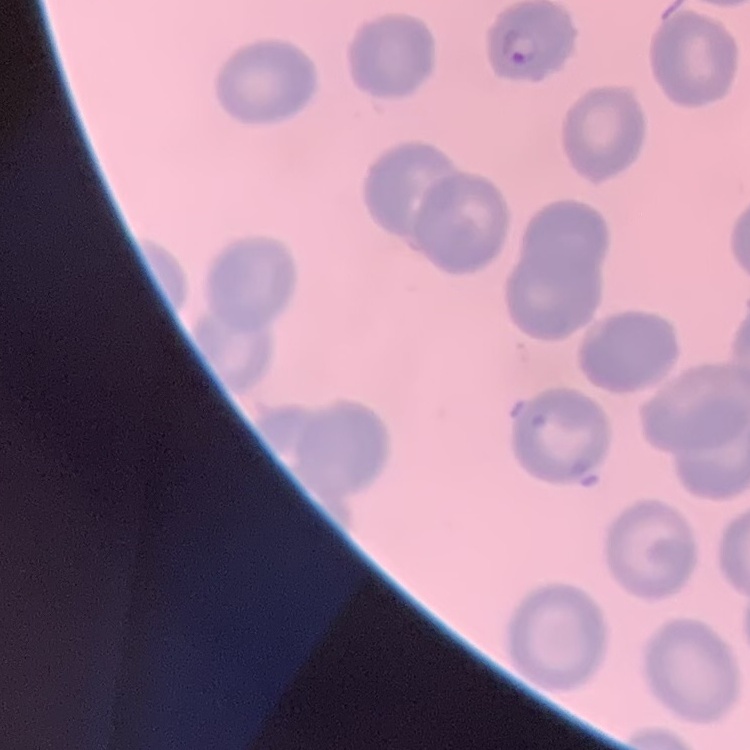

The erythrocytes show no rouleaux formation. One tile cut from a larger photomicrograph. Thin blood film. Stained with either Field's or Giemsa.